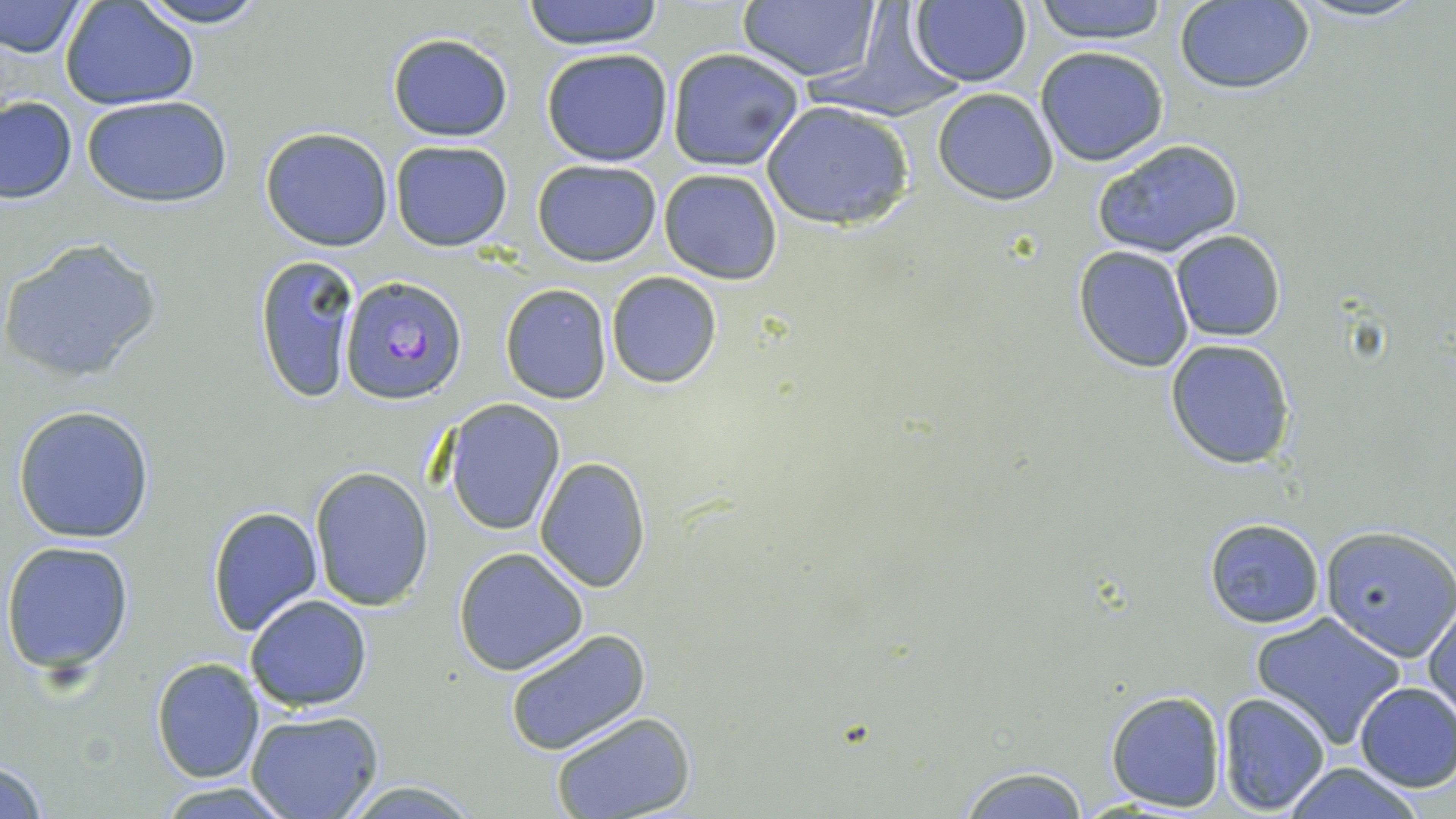
{
  "slide_level_diagnosis": "Plasmodium falciparum",
  "modality": "light microscopy",
  "field_of_view": "single",
  "preparation": "thin blood film",
  "plasmodium_falciparum_infected_red_blood_cell_locations": "approximate bounding boxes as named x1/y1/x2/y2 corners in pixels: (x1=341, y1=274, x2=469, y2=405)",
  "magnification": "1000x",
  "uninfected_red_blood_cell_locations": "approximate bounding boxes as named x1/y1/x2/y2 corners in pixels: (x1=0, y1=0, x2=86, y2=60), (x1=129, y1=0, x2=273, y2=27), (x1=519, y1=0, x2=668, y2=49), (x1=736, y1=0, x2=884, y2=84), (x1=804, y1=0, x2=967, y2=123), (x1=1030, y1=0, x2=1171, y2=45), (x1=1287, y1=0, x2=1433, y2=23), (x1=909, y1=1, x2=1032, y2=87), (x1=1173, y1=1, x2=1314, y2=94), (x1=61, y1=2, x2=200, y2=109), (x1=386, y1=32, x2=513, y2=142), (x1=1033, y1=45, x2=1170, y2=167), (x1=666, y1=46, x2=805, y2=171), (x1=540, y1=48, x2=674, y2=167), (x1=932, y1=87, x2=1059, y2=205), (x1=1, y1=96, x2=76, y2=203), (x1=80, y1=96, x2=233, y2=206), (x1=761, y1=100, x2=916, y2=231), (x1=260, y1=127, x2=394, y2=250), (x1=1092, y1=138, x2=1245, y2=259), (x1=389, y1=139, x2=513, y2=251), (x1=532, y1=160, x2=661, y2=266), (x1=659, y1=168, x2=782, y2=283), (x1=1170, y1=229, x2=1287, y2=343), (x1=1, y1=235, x2=163, y2=383), (x1=1074, y1=245, x2=1196, y2=372), (x1=253, y1=252, x2=360, y2=403), (x1=606, y1=272, x2=722, y2=388), (x1=500, y1=283, x2=611, y2=403), (x1=1165, y1=338, x2=1296, y2=470), (x1=444, y1=400, x2=566, y2=537), (x1=12, y1=405, x2=156, y2=544), (x1=534, y1=456, x2=652, y2=592), (x1=309, y1=467, x2=434, y2=613), (x1=206, y1=505, x2=323, y2=637), (x1=1201, y1=517, x2=1324, y2=631), (x1=1320, y1=526, x2=1456, y2=661), (x1=3, y1=539, x2=135, y2=675), (x1=453, y1=548, x2=589, y2=677), (x1=245, y1=594, x2=372, y2=712), (x1=1426, y1=602, x2=1456, y2=718), (x1=1251, y1=613, x2=1407, y2=749), (x1=504, y1=629, x2=651, y2=757), (x1=151, y1=658, x2=266, y2=784), (x1=1353, y1=681, x2=1456, y2=793), (x1=1105, y1=688, x2=1226, y2=812), (x1=1217, y1=692, x2=1332, y2=815), (x1=246, y1=710, x2=385, y2=819), (x1=550, y1=711, x2=698, y2=819), (x1=0, y1=758, x2=51, y2=817), (x1=951, y1=762, x2=1097, y2=819), (x1=1283, y1=763, x2=1427, y2=818), (x1=337, y1=782, x2=481, y2=816), (x1=156, y1=783, x2=293, y2=816)",
  "image_size": "1456×819 pixels",
  "stain": "May-Grünwald-Giemsa"
}